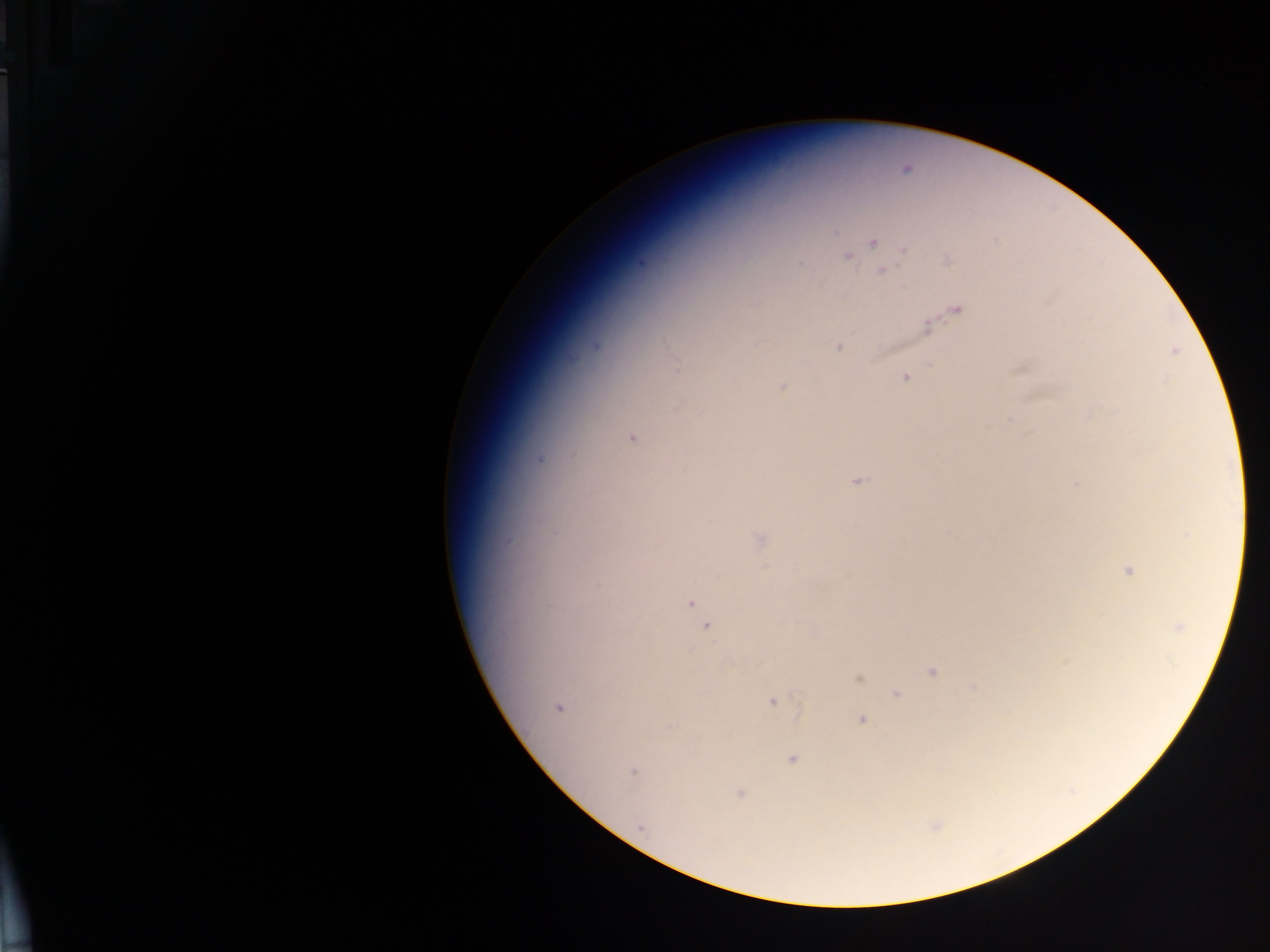
Approximate centers as {x, y} in pixels.
Summary:
  - Plasmodium parasite locations: {906, 168}, {872, 241}, {904, 249}, {848, 256}, {948, 260}, {881, 270}, {955, 309}, {926, 327}, {594, 345}, {837, 346}, {1174, 350}, {676, 364}, {905, 376}, {782, 387}, {631, 437}, {540, 459}, {856, 479}, {760, 539}, {1128, 571}, {690, 602}, {705, 625}, {1178, 627}, {1066, 661}, {933, 671}, {858, 677}, {974, 686}, {895, 694}, {772, 701}, {557, 708}, {861, 718}, {791, 758}, {632, 771}, {739, 793}, {639, 826}, {934, 826}
  - Capture: mobile-phone photograph through a microscope
  - Country: Ghana
  - Image size: 1270×952 pixels
  - Preparation: thick blood smear
  - Field of view: single